Locate every Plasmodium parasite.
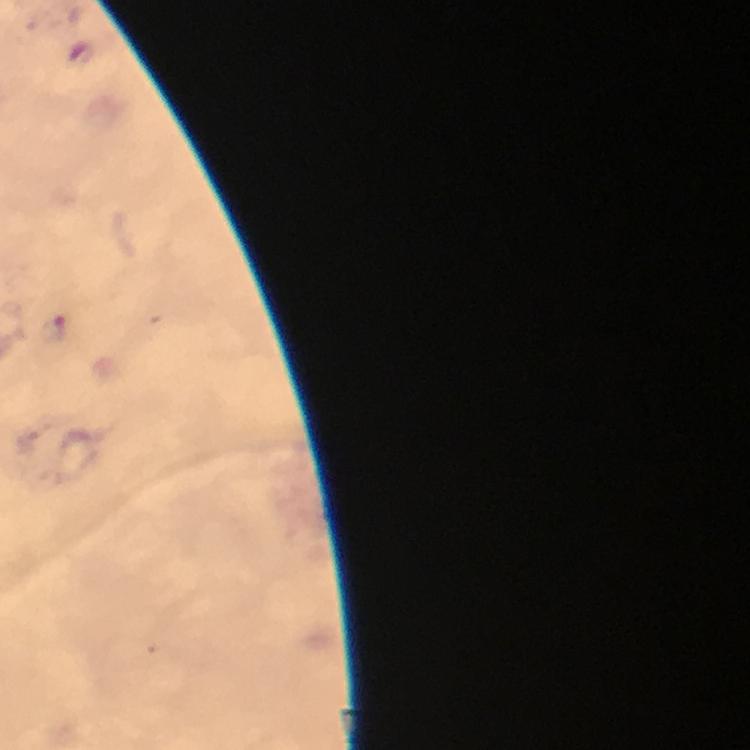

Approximate object centers, in pixels from the top-left corner.
Plasmodium parasites: (x=57, y=331), (x=28, y=442).

Cropped region of a single field of view. Thick smear. Image is 750×750 pixels. At 100x magnification. Giemsa stain. Smartphone photograph taken through a microscope. From a malaria diagnostic workup. Immersion oil applied.